Assess this cell for malaria.
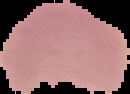
Parasitized.

Image is 130×94 pixels. From a thin blood film. Segmented cell region on a black background.